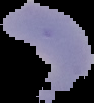

Summary:
  - Image type: cell region segmented out of the field of view; surrounding area masked to black
  - Malaria status: parasitized
  - Image size: 94×103 pixels
  - Preparation: thin blood film